Identify the blood parasite species.
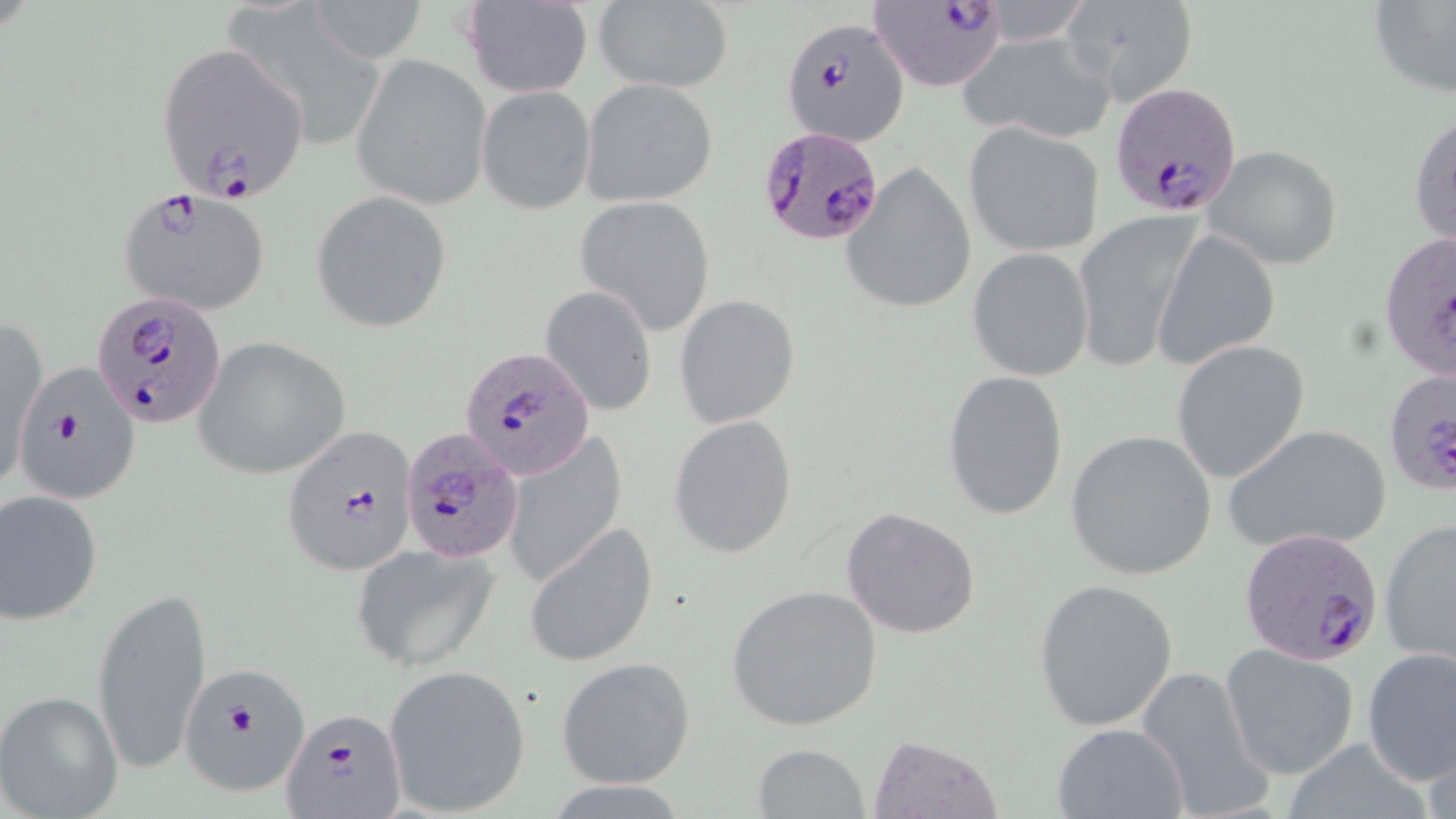
Plasmodium falciparum.

preparation = thin blood film
uninfected red blood cell locations = approximate bounding boxes as (x1,y1)-(x2,y2) corner pairs in pixels: (308,0)-(428,65), (592,0)-(734,93), (1063,0)-(1196,104), (1369,0)-(1456,100), (461,1)-(593,97), (958,31)-(1114,142), (353,55)-(491,209), (580,79)-(719,206), (477,86)-(596,214), (1409,110)-(1456,253), (964,123)-(1106,256), (1202,145)-(1344,270), (841,161)-(978,315), (312,190)-(452,333), (575,195)-(716,336), (1071,211)-(1202,372), (1155,228)-(1280,369), (967,248)-(1094,380), (540,285)-(658,416), (674,294)-(800,427), (1,318)-(47,495), (193,337)-(350,479), (1172,340)-(1310,483), (942,370)-(1069,520), (668,415)-(798,559), (1223,423)-(1393,555), (501,429)-(627,586), (1065,429)-(1219,582), (0,490)-(103,624), (840,506)-(981,639), (1381,515)-(1456,666), (523,524)-(658,667), (353,544)-(499,670), (1034,578)-(1177,732), (725,584)-(885,731), (92,585)-(213,777), (1222,643)-(1359,778), (1360,645)-(1455,788), (557,656)-(697,788), (383,665)-(531,816), (1134,666)-(1273,819), (0,688)-(124,818), (1050,722)-(1190,818), (868,733)-(1002,818), (752,742)-(870,817)
stain = May-Grünwald-Giemsa
field of view = one of a larger specimen
Plasmodium falciparum-infected red blood cell locations = approximate bounding boxes as (x1,y1)-(x2,y2) corner pairs in pixels: (869,0)-(1009,92), (781,15)-(911,144), (153,40)-(312,208), (1110,82)-(1244,216), (757,125)-(887,246), (117,187)-(271,317), (1379,231)-(1454,383), (93,292)-(227,430), (462,346)-(595,481), (12,363)-(142,508), (1383,368)-(1456,496), (282,424)-(420,578), (402,428)-(525,563), (1240,529)-(1386,664), (174,661)-(314,799), (282,707)-(407,819)
magnification = 1000x
modality = optical microscopy
image size = 1456×819 pixels